Locate every Plasmodium parasite by life-cycle stage, and every leukocyte.
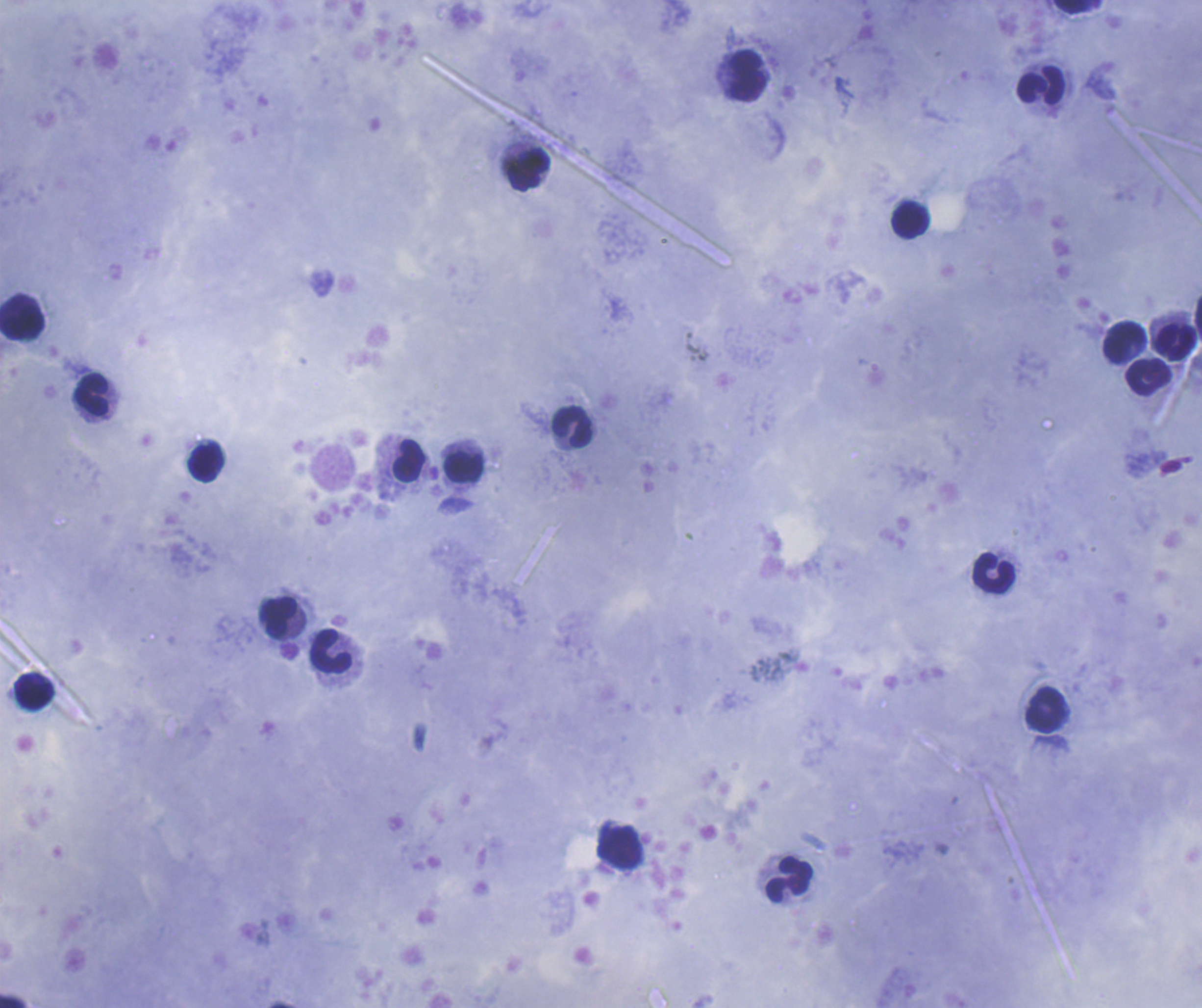

No Plasmodium parasites seen.
Approximate centers as {x, y} in pixels.
Leukocytes: {1072, 7}, {747, 76}, {1041, 85}, {529, 170}, {910, 220}, {24, 323}, {1123, 342}, {1175, 342}, {1148, 375}, {91, 394}, {572, 426}, {409, 461}, {205, 462}, {464, 466}, {993, 573}, {278, 617}, {330, 652}, {34, 694}, {1045, 709}, {619, 846}, {789, 879}, {13, 1001}.

Summary:
  - Stain: Romanowsky
  - Context: previously used in a real diagnosis
  - Preparation: thick blood film
  - Coloration quality: good
  - Background quality: good
  - Magnification: 100x
  - Field of view: one from this slide
  - Image size: 1202×1008 pixels